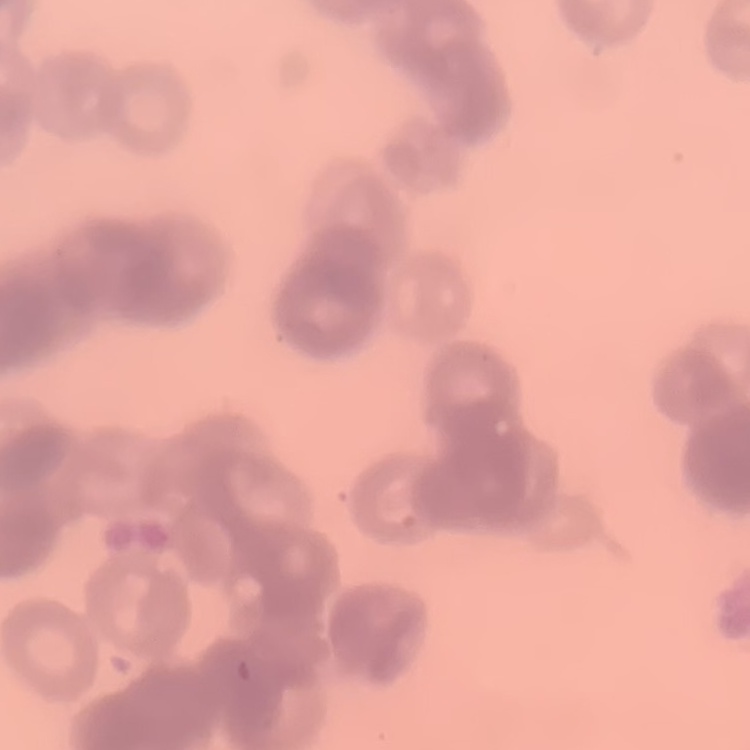

Summary:
  - Red blood cell morphology: rouleaux formation
  - Preparation: thin blood smear
  - Stain: Field's or Giemsa
  - Image type: square crop of a larger photomicrograph